Report the malaria status of this cell.
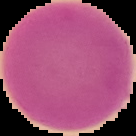

Uninfected.

Summary:
  - Image size: 136×136 pixels
  - Preparation: thin blood smear
  - Image type: segmented cell region on a black background